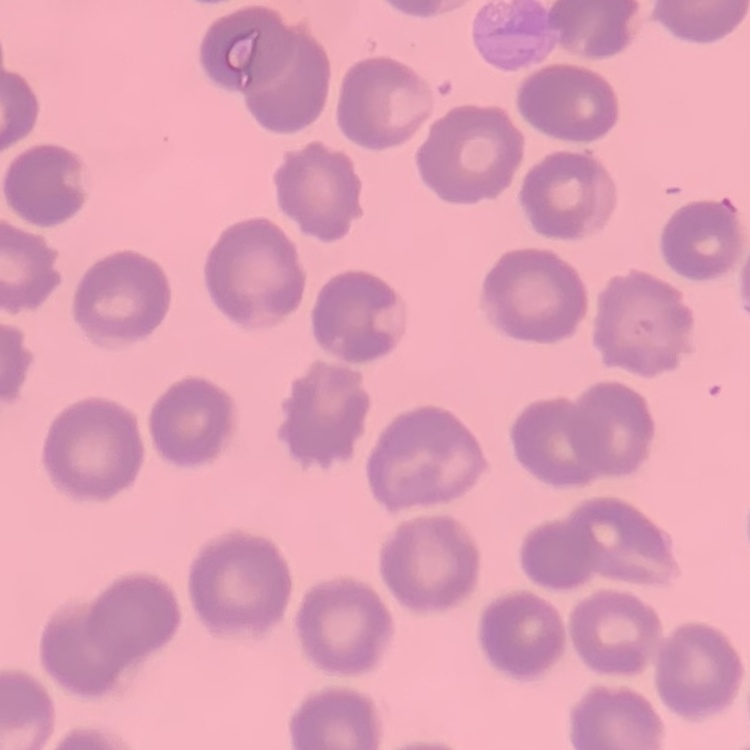

Summary:
  - Erythrocyte morphology: no rouleaux formation
  - Preparation: thin blood smear
  - Image type: one tile cut from a larger photomicrograph
  - Stain: Field's or Giemsa